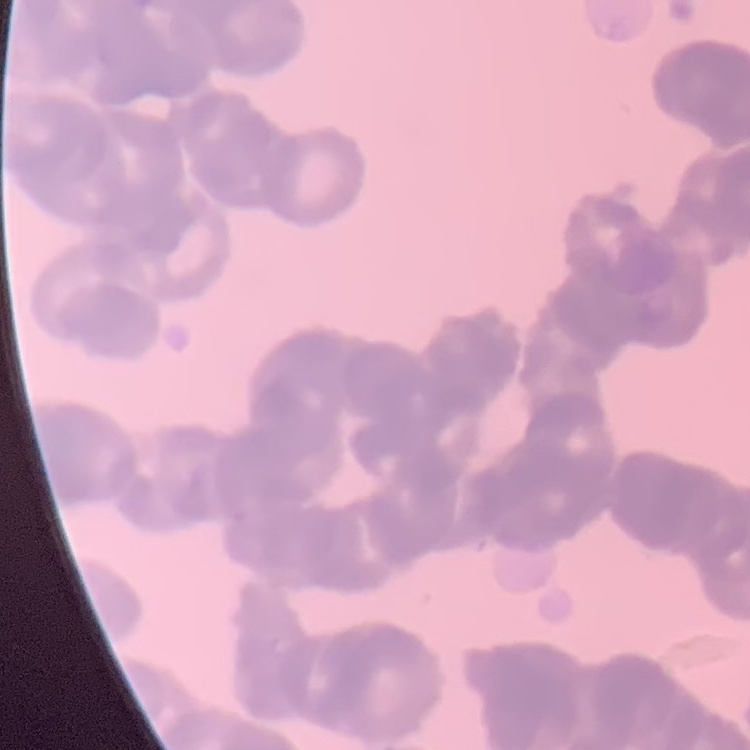
erythrocyte morphology = rouleaux formation
preparation = thin blood smear
stain = Field's or Giemsa
image type = one tile cut from a larger photomicrograph